Give the position of every Plasmodium parasite visible.
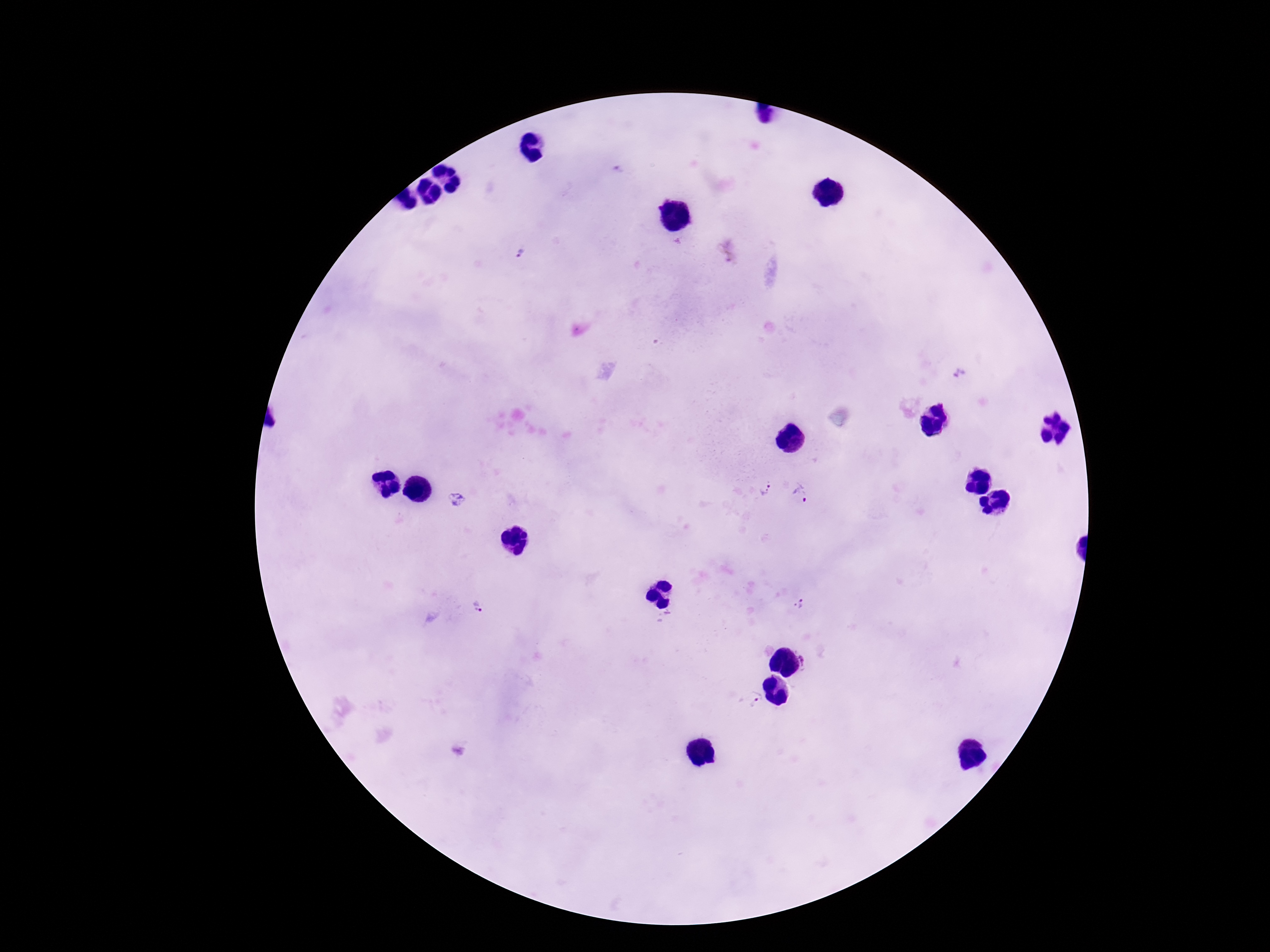

Approximate centers as (x, y) in pixels.
Plasmodium parasites: (520, 253), (959, 373), (764, 489), (799, 493), (457, 500), (800, 602), (477, 608), (805, 658), (754, 699).

patient malaria status = infected
capture = smartphone camera through the microscope eyepiece
stain = Giemsa
image size = 1270×952 pixels
field of view = single
magnification = 100x
preparation = thick blood film